Assess the morphology of the red blood cells.
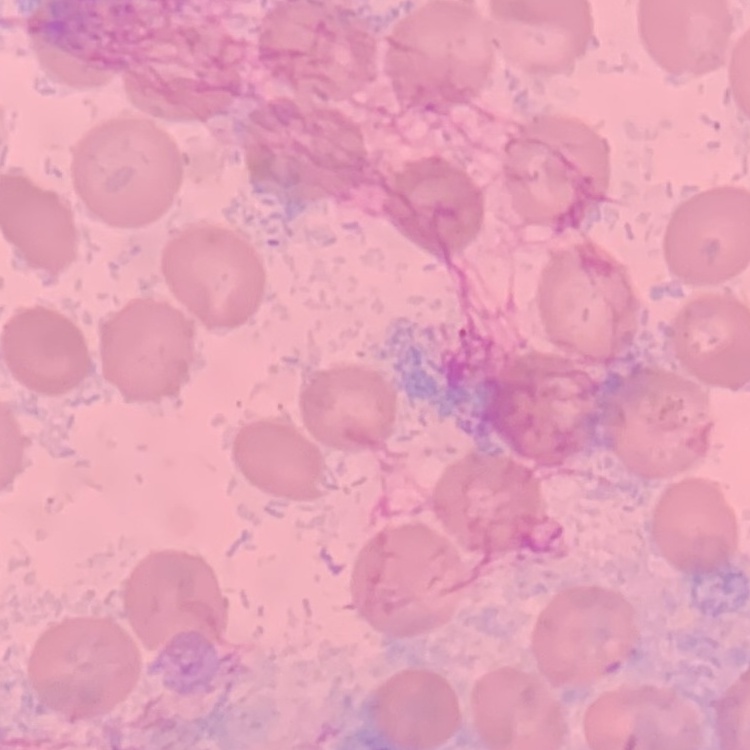
No rouleaux formation.

{
  "image_type": "square crop of a larger photomicrograph",
  "preparation": "thin blood smear",
  "stain": "Field's or Giemsa"
}